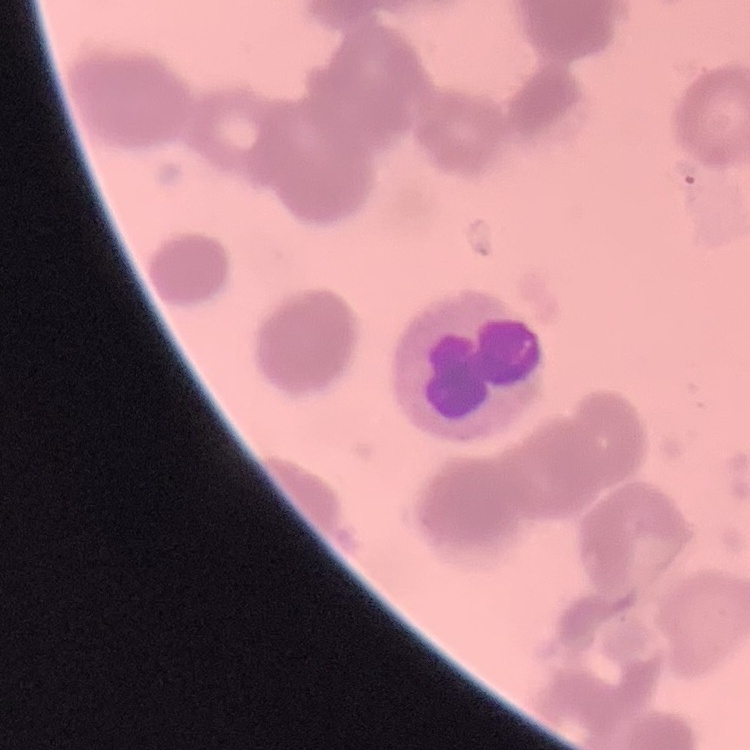
{
  "red_blood_cell_morphology": "rouleaux formation",
  "image_type": "square crop of a larger photomicrograph",
  "preparation": "thin blood film",
  "stain": "Field's or Giemsa"
}